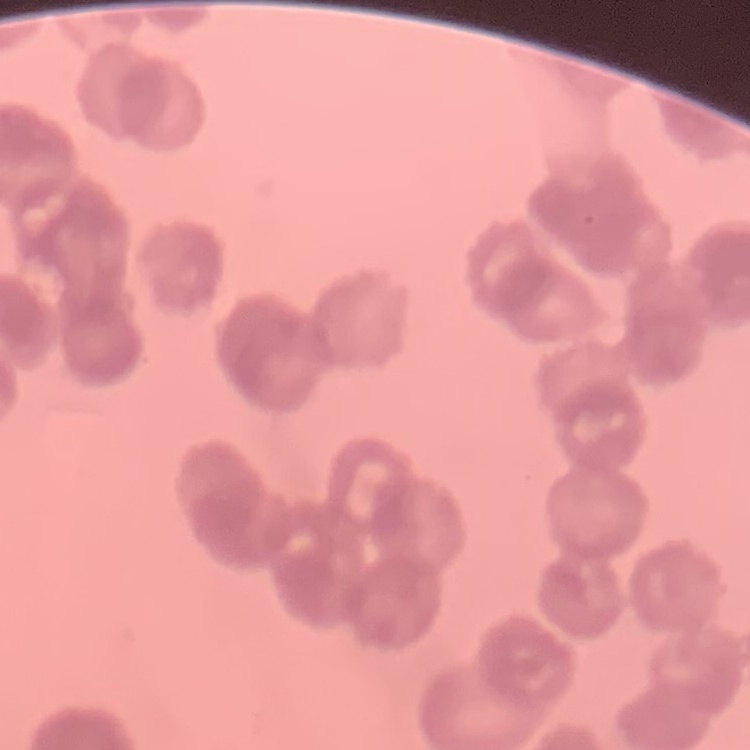
erythrocyte morphology = rouleaux formation
preparation = thin blood film
image type = one tile cut from a larger photomicrograph
stain = Field's or Giemsa